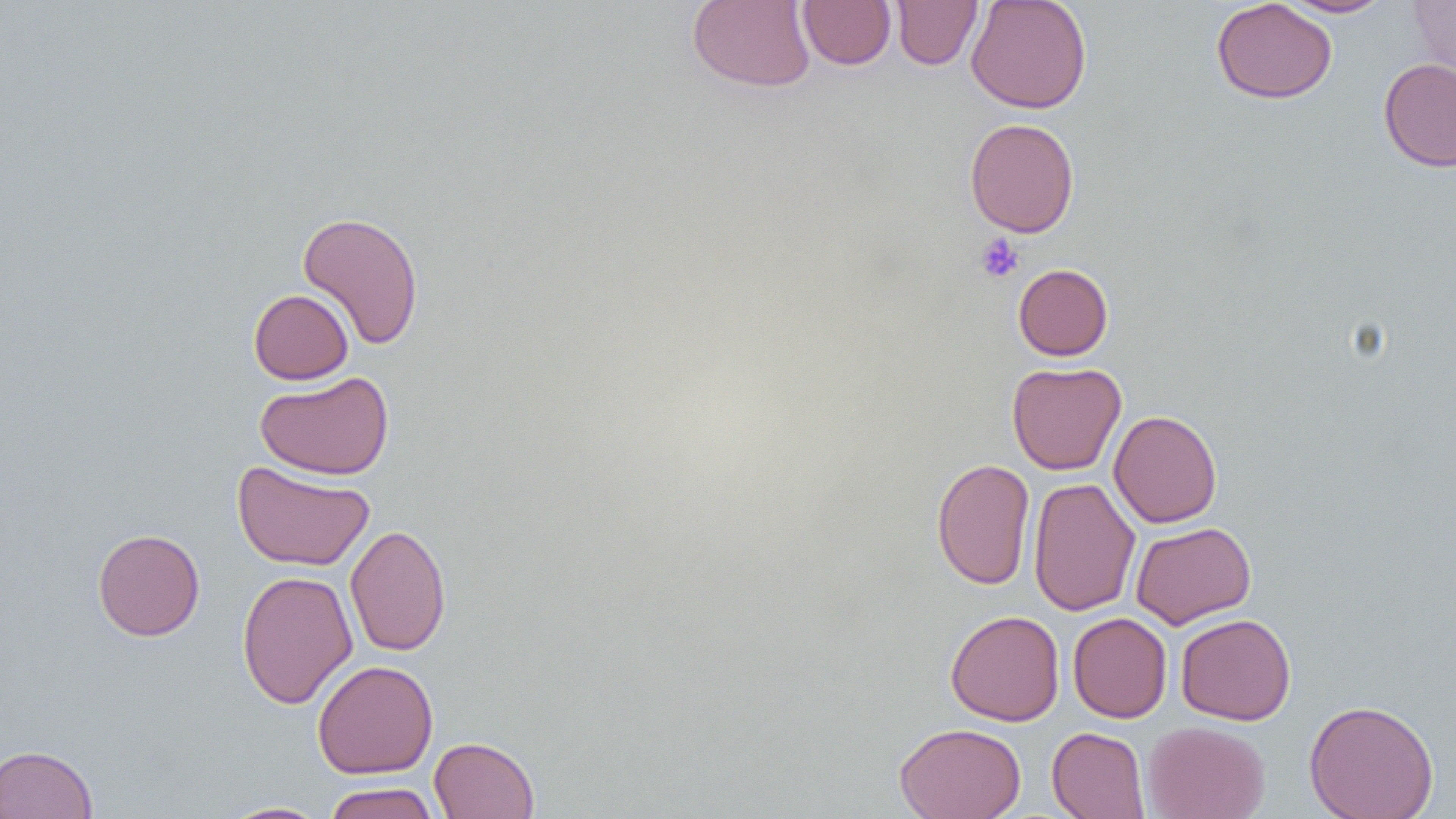
Approximate bounding boxes as [x1, y1, x2, y2] in pixels. Platelet locations: [975, 233, 1025, 283]. Uninfected red blood cell locations: [687, 0, 816, 92], [797, 0, 896, 70], [965, 0, 1092, 114], [1212, 0, 1337, 104], [1278, 0, 1395, 18], [891, 1, 982, 70], [1407, 1, 1456, 82], [1378, 58, 1456, 172], [964, 118, 1079, 237], [297, 211, 424, 350], [1013, 263, 1113, 360], [248, 289, 354, 385], [1007, 361, 1127, 475], [255, 371, 394, 480], [1109, 410, 1222, 528], [931, 458, 1036, 590], [232, 460, 375, 571], [1028, 477, 1141, 617], [1130, 521, 1256, 629], [345, 523, 451, 657], [92, 528, 205, 641], [237, 570, 358, 709], [945, 610, 1065, 726], [1068, 612, 1172, 723], [1176, 613, 1296, 725], [312, 660, 438, 779], [1304, 698, 1440, 819], [1142, 720, 1270, 819], [894, 722, 1026, 819], [1046, 726, 1150, 819], [429, 736, 540, 819], [0, 743, 98, 819], [323, 782, 440, 819], [217, 801, 331, 819]. Slide-level diagnosis: negative for blood parasites. Captured at 1000x magnification. Optical microscopy. Image is 1456×819 pixels. Single field of view. Thin blood film.